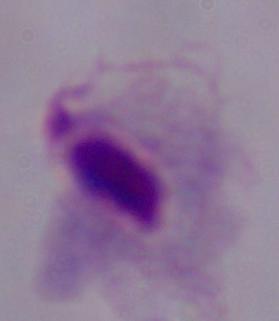
Summary:
  - Identification: trichomonad
  - Modality: micrograph
  - Magnification: 1000x